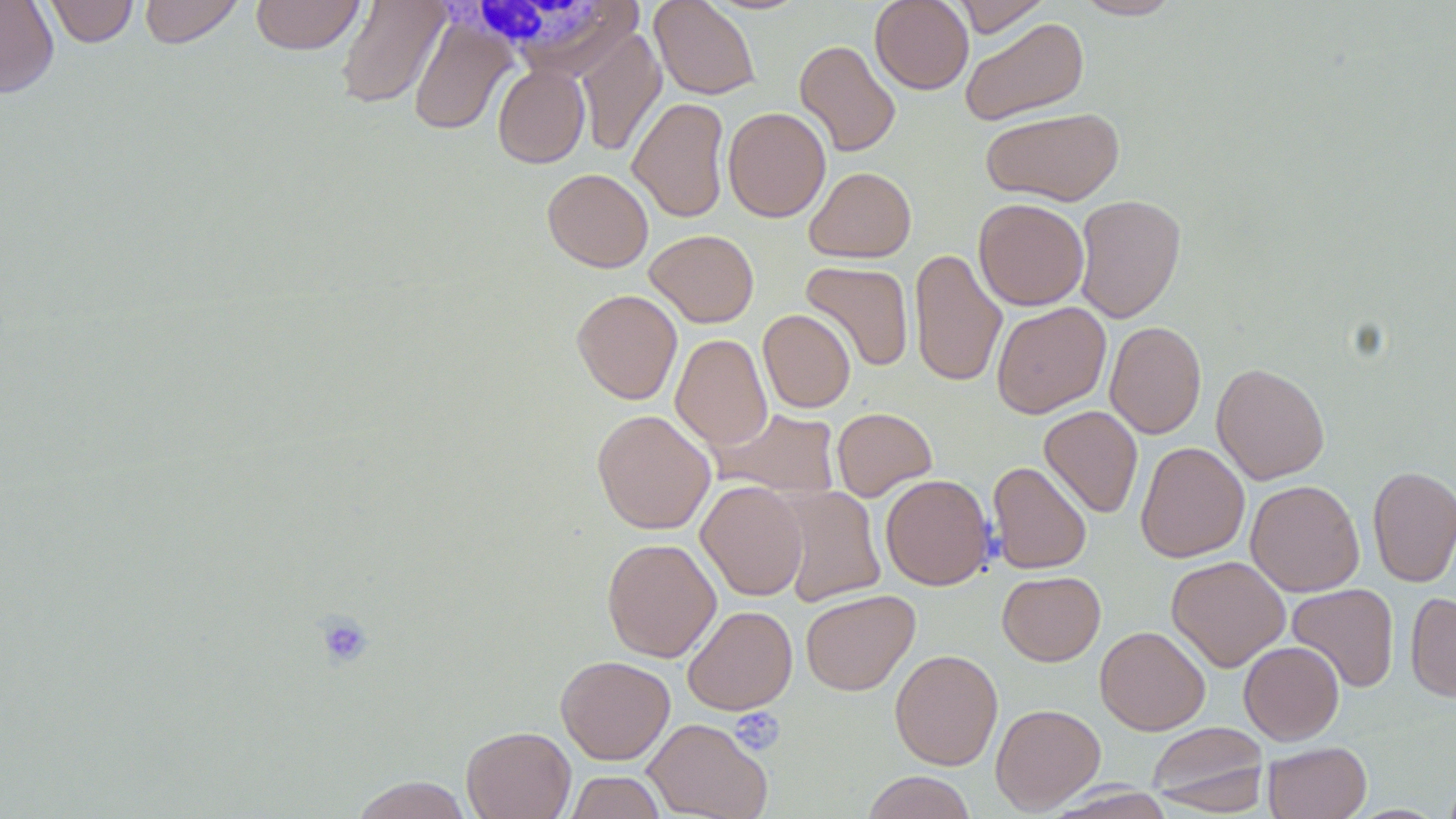
Summary:
  - Coordinate format: approximate bounding boxes as [x1, y1, x2, y2] in pixels
  - White blood cell locations: [438, 2, 614, 60]
  - Uninfected red blood cell locations: [0, 0, 59, 99], [43, 0, 139, 47], [139, 0, 245, 48], [250, 0, 365, 54], [335, 0, 450, 110], [649, 0, 761, 100], [870, 0, 973, 94], [950, 0, 1052, 37], [1072, 0, 1184, 20], [409, 13, 516, 136], [959, 16, 1090, 126], [575, 29, 667, 156], [794, 40, 901, 157], [493, 64, 590, 168], [628, 97, 731, 223], [723, 106, 830, 223], [980, 107, 1125, 206], [805, 166, 916, 263], [542, 168, 653, 272], [1073, 194, 1186, 323], [973, 198, 1089, 310], [645, 229, 759, 327], [909, 248, 1007, 388], [800, 260, 914, 372], [571, 289, 682, 404], [992, 302, 1110, 419], [758, 309, 856, 413], [1105, 320, 1206, 439], [671, 334, 772, 452], [1211, 362, 1330, 485], [1040, 405, 1143, 518], [831, 407, 938, 501], [713, 408, 842, 498], [592, 409, 715, 535], [1135, 441, 1250, 563], [987, 460, 1091, 574], [1368, 465, 1456, 587], [880, 474, 994, 590], [1245, 479, 1364, 597], [696, 480, 808, 601], [774, 486, 886, 607], [602, 537, 721, 662], [1167, 555, 1290, 671], [997, 570, 1106, 665], [1287, 583, 1399, 693], [799, 589, 920, 696], [1406, 592, 1456, 702], [682, 605, 797, 715], [1095, 625, 1210, 735], [1238, 641, 1344, 745], [889, 649, 1003, 770], [555, 655, 675, 764], [990, 703, 1105, 813], [643, 718, 772, 819], [1146, 721, 1271, 815], [461, 726, 576, 819], [1263, 741, 1372, 819], [565, 771, 666, 819], [861, 771, 977, 819], [351, 775, 472, 818]
  - Platelet locations: [314, 612, 374, 669], [729, 708, 785, 756]
  - Slide-level diagnosis: negative for blood parasites
  - Field of view: single
  - Preparation: thin blood smear
  - Stain: May-Grünwald-Giemsa
  - Modality: optical microscopy
  - Magnification: 1000x
  - Image size: 1456×819 pixels